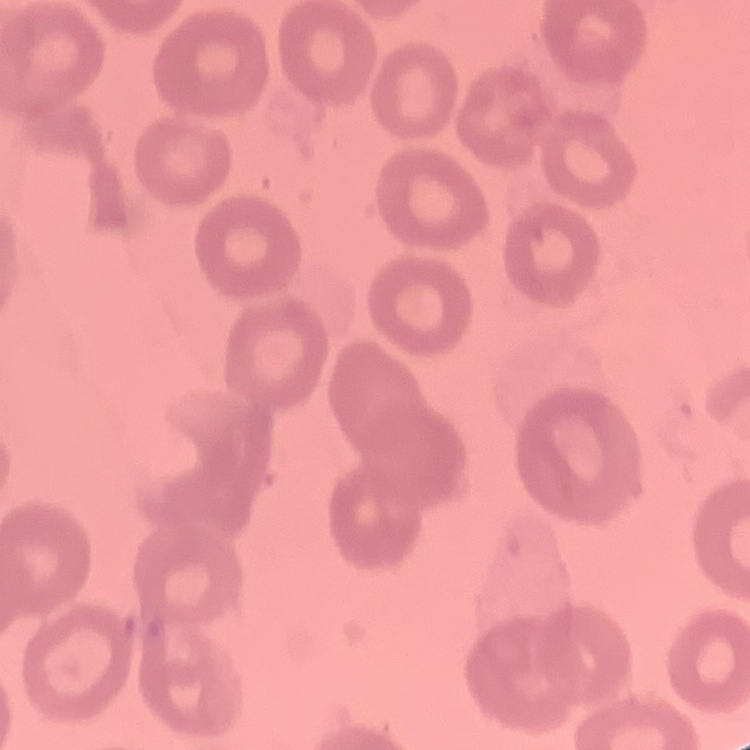
erythrocyte_morphology: no rouleaux formation
image_type: one tile cut from a larger photomicrograph
stain: Field's or Giemsa
preparation: thin blood film